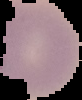

Malaria status: parasitized. Image is 82×100 pixels. From a thin blood smear. The area outside the segmented cell region is set to black.